Describe the morphology of the erythrocytes.
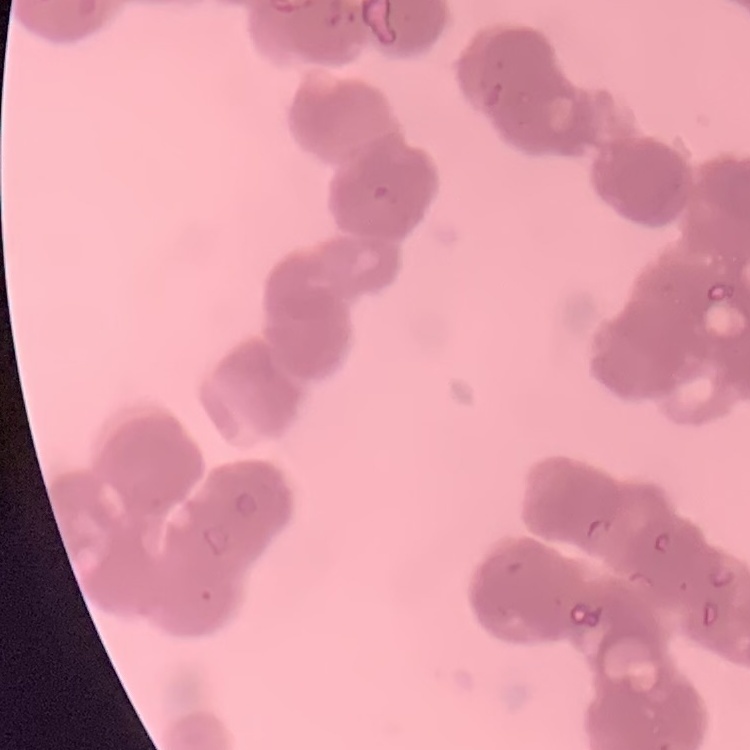

Rouleaux formation.

preparation: thin blood film
image_type: square crop of a larger photomicrograph
stain: Field's or Giemsa